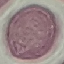 Malaria status: uninfected. Acquired by smartphone through the microscope eyepiece. Giemsa-stained preparation. Thin blood smear. Automatically extracted cell patch, resized to 64 × 64 pixels.